Report the malaria status of this cell.
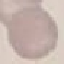

It is uninfected.

{
  "stain": "Giemsa",
  "capture": "smartphone camera at the microscope eyepiece",
  "image_type": "automatically extracted cell patch, resized to 64 × 64 pixels",
  "preparation": "thin blood film"
}